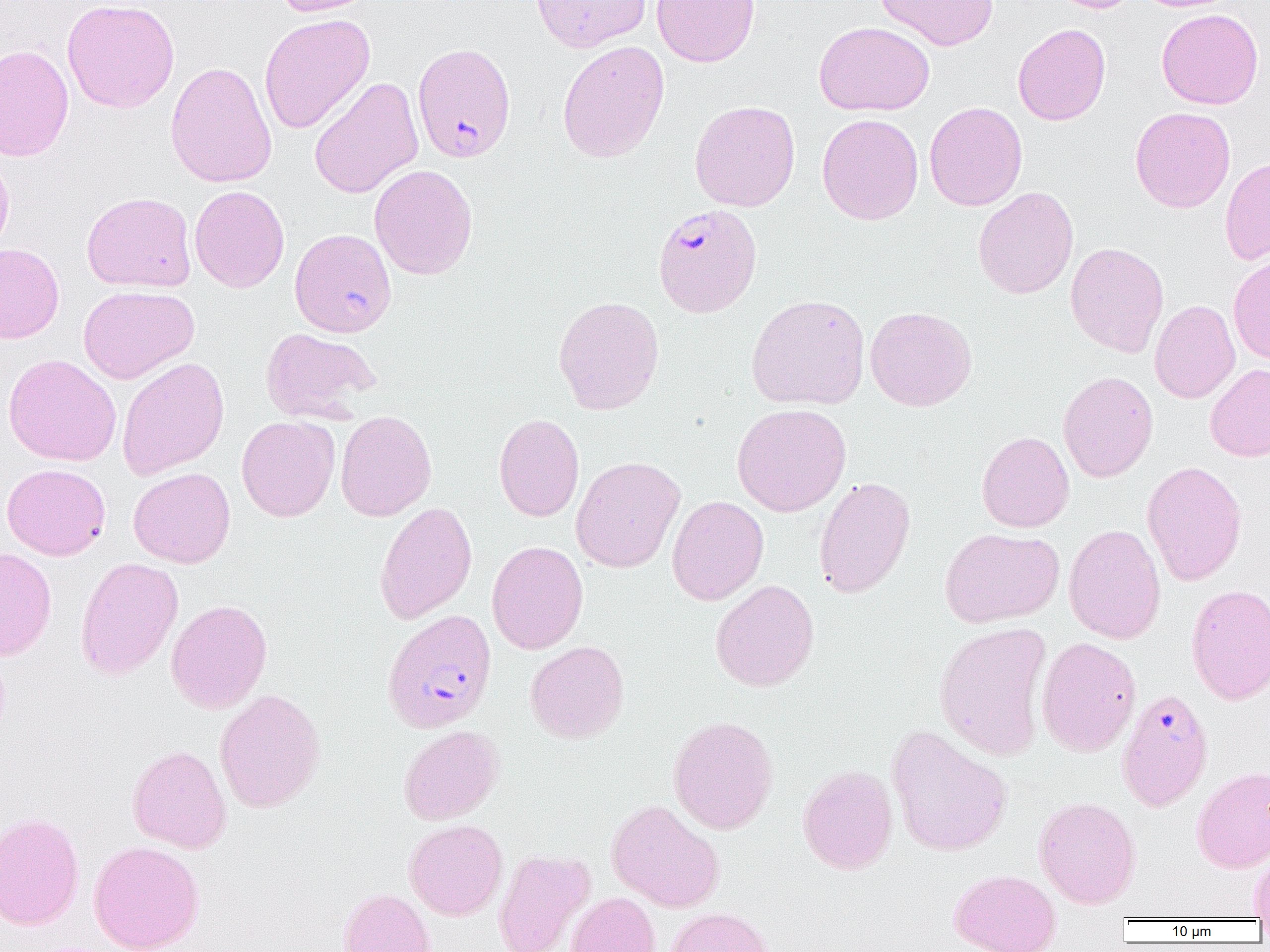 Approximate bounding boxes as (x1, y1, x2, y2) in pixels. Plasmodium falciparum-infected red blood cell locations: (412, 42, 516, 162), (652, 203, 762, 317), (382, 608, 497, 733), (1116, 689, 1214, 811). Uninfected red blood cell locations: (61, 0, 180, 113), (272, 0, 376, 17), (531, 0, 651, 53), (651, 0, 760, 67), (875, 0, 998, 50), (1050, 0, 1141, 13), (1156, 8, 1264, 109), (259, 14, 375, 134), (814, 21, 934, 115), (1012, 23, 1111, 125), (557, 40, 670, 163), (0, 44, 74, 162), (165, 61, 277, 188), (309, 77, 424, 199), (689, 100, 800, 212), (924, 101, 1028, 211), (1130, 106, 1235, 213), (817, 113, 924, 225), (0, 150, 14, 258), (1220, 156, 1270, 266), (369, 164, 478, 280), (189, 185, 289, 293), (973, 187, 1078, 299), (82, 191, 197, 293), (289, 228, 397, 337), (1065, 242, 1169, 358), (0, 243, 64, 343), (1228, 254, 1270, 365), (78, 285, 199, 384), (746, 294, 870, 410), (553, 295, 665, 415), (1150, 300, 1240, 403), (865, 306, 977, 411), (260, 327, 381, 423), (3, 354, 121, 466), (117, 356, 229, 480), (1205, 363, 1270, 462), (1057, 370, 1158, 482), (732, 403, 851, 516), (335, 410, 437, 521), (494, 413, 584, 522), (236, 416, 340, 522), (976, 431, 1074, 533), (570, 456, 685, 573), (1141, 461, 1247, 585), (2, 463, 111, 560), (128, 467, 235, 568), (813, 476, 916, 599), (667, 495, 768, 606), (374, 501, 477, 624), (1064, 523, 1166, 644), (939, 527, 1064, 627), (486, 540, 588, 654), (0, 548, 57, 660), (75, 557, 183, 680), (710, 579, 820, 692), (1185, 584, 1270, 705), (166, 599, 273, 714), (934, 621, 1053, 761), (1036, 636, 1141, 758), (525, 641, 630, 743), (214, 688, 326, 813), (668, 715, 779, 834), (398, 725, 503, 825), (886, 725, 1013, 857), (127, 744, 231, 853), (797, 764, 898, 874), (1192, 766, 1270, 872), (1034, 796, 1141, 909), (606, 799, 725, 913), (0, 811, 85, 930), (404, 819, 507, 920), (88, 840, 204, 952), (494, 849, 595, 952), (1249, 854, 1270, 919), (949, 869, 1061, 952), (338, 887, 436, 952), (565, 892, 660, 952), (666, 906, 776, 952). Slide-level diagnosis: Plasmodium falciparum. Image is 1270×952 pixels. Thin blood smear. Optical microscopy. 1000x magnification. Single field of view.